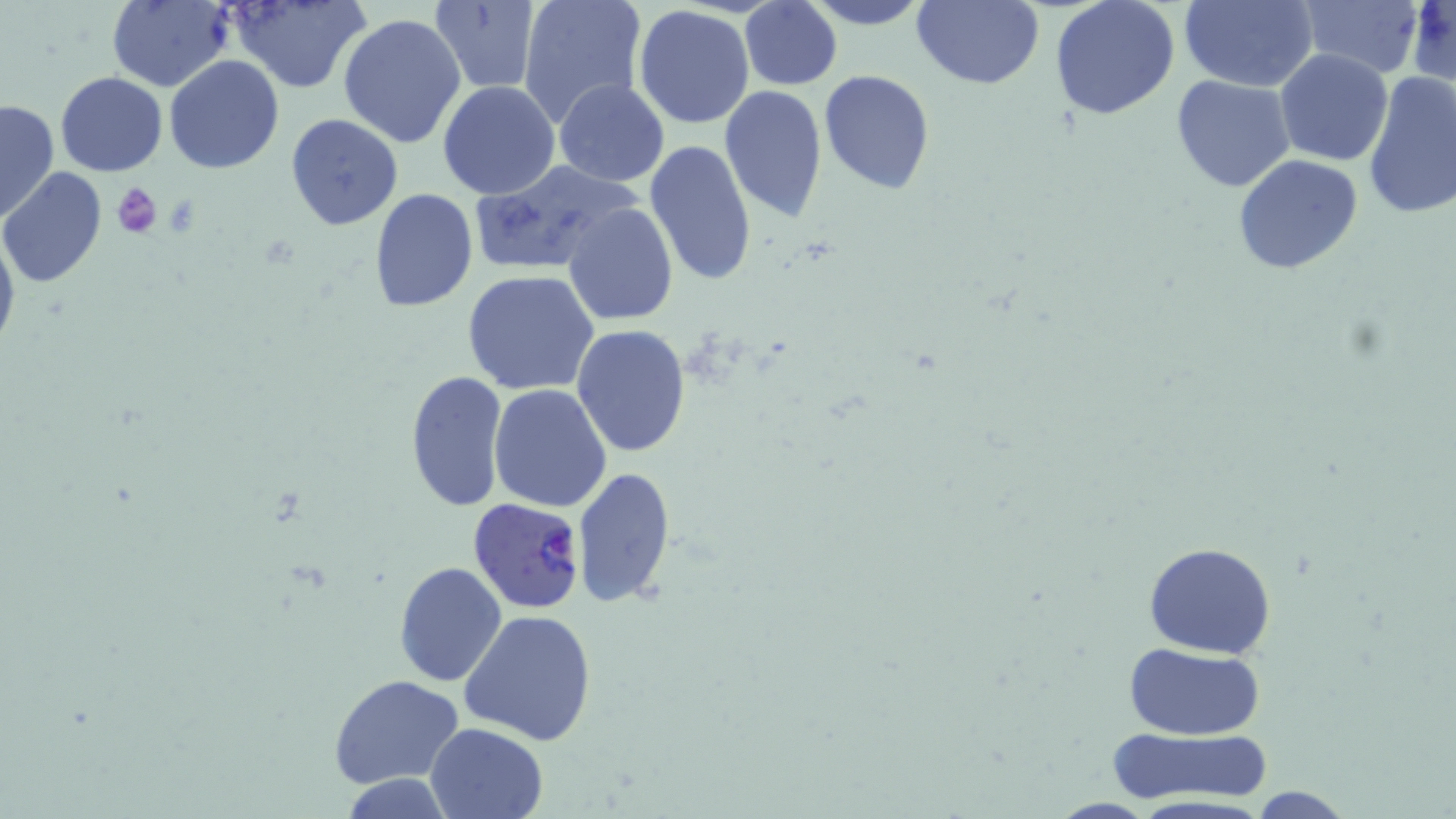

plasmodium_falciparum_infected_red_blood_cell_locations: 'approximate bounding boxes as (x1,y1)-(x2,y2) corner pairs in pixels: (468,496)-(586,612)'
slide_level_diagnosis: Plasmodium falciparum
preparation: thin blood film
field_of_view: single
magnification: 1000x
stain: May-Grünwald-Giemsa
uninfected_red_blood_cell_locations: 'approximate bounding boxes as (x1,y1)-(x2,y2) corner pairs in pixels: (226,0)-(370,92), (517,0)-(647,127), (800,0)-(936,29), (910,0)-(1043,89), (1048,0)-(1180,121), (1179,0)-(1318,92), (1297,0)-(1423,78), (105,1)-(233,90), (428,1)-(542,92), (739,2)-(840,90), (632,5)-(756,128), (336,11)-(466,150), (1274,47)-(1394,166), (164,54)-(285,173), (819,69)-(936,195), (55,71)-(168,178), (1361,72)-(1456,222), (1170,73)-(1296,192), (554,79)-(671,186), (438,81)-(561,200), (719,85)-(828,223), (1,98)-(59,226), (285,112)-(404,232), (643,140)-(758,289), (1232,154)-(1363,275), (465,160)-(637,278), (1,167)-(107,287), (368,189)-(478,312), (563,202)-(680,326), (0,220)-(20,361), (461,269)-(601,395), (571,324)-(691,457), (403,370)-(510,513), (489,384)-(612,513), (572,467)-(676,611), (1142,541)-(1278,659), (392,560)-(507,686), (460,609)-(597,744), (1121,643)-(1266,741), (328,675)-(464,790), (425,721)-(549,819), (1110,728)-(1274,806), (1241,786)-(1359,818)'
image_size: 1456×819 pixels
platelet_locations: 'approximate bounding boxes as (x1,y1)-(x2,y2) corner pairs in pixels: (111,183)-(163,237)'
modality: light microscopy